Assess this cell for malaria.
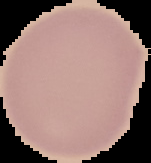
It is uninfected.

From a thin blood smear. Image is 151×163 pixels. The area outside the segmented cell region is set to black.